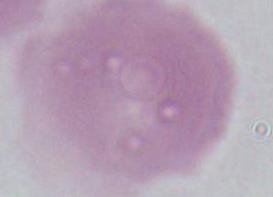

identification: red blood cell
modality: photomicrograph
magnification: 1000x